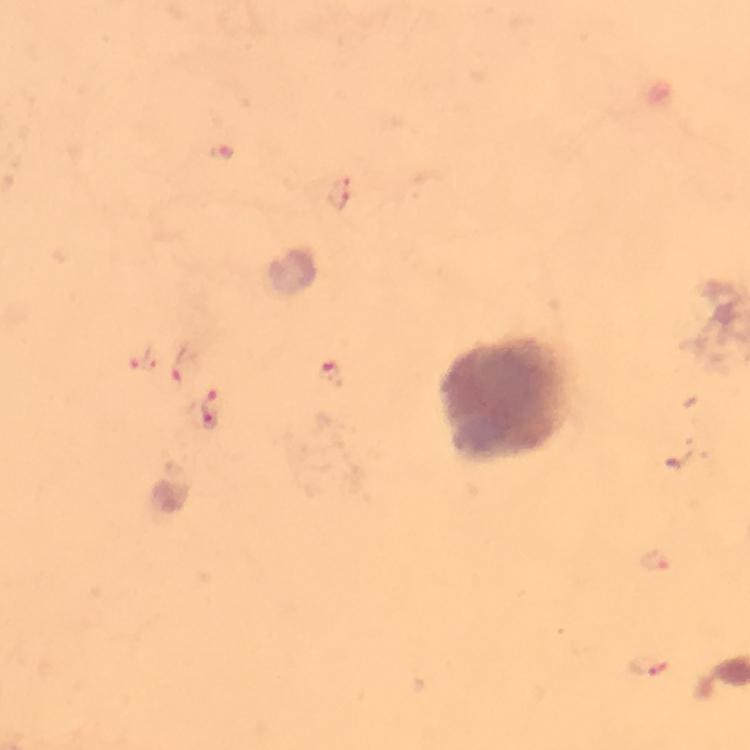

Approximate object centers, in pixels from the top-left corner.
Summary:
  - Leukocyte locations: (x=505, y=396)
  - Malaria parasite locations: (x=142, y=361), (x=183, y=366), (x=334, y=375), (x=212, y=408), (x=655, y=561), (x=647, y=668)
  - Immersion oil: applied
  - Cropped from: a single field of view
  - Preparation: thick blood film
  - Magnification: 100x
  - Context: from a diagnostic examination for malaria
  - Capture: smartphone mounted on the microscope
  - Stain: Giemsa
  - Image size: 750×750 pixels